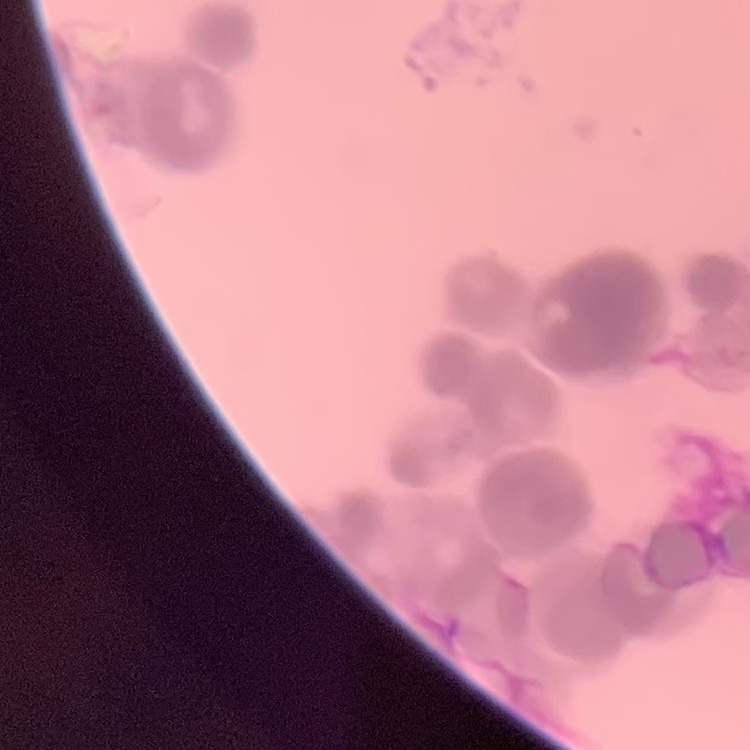

Summary:
  - Red blood cell morphology: rouleaux formation
  - Image type: square crop of a larger photomicrograph
  - Stain: Field's or Giemsa
  - Preparation: thin blood smear